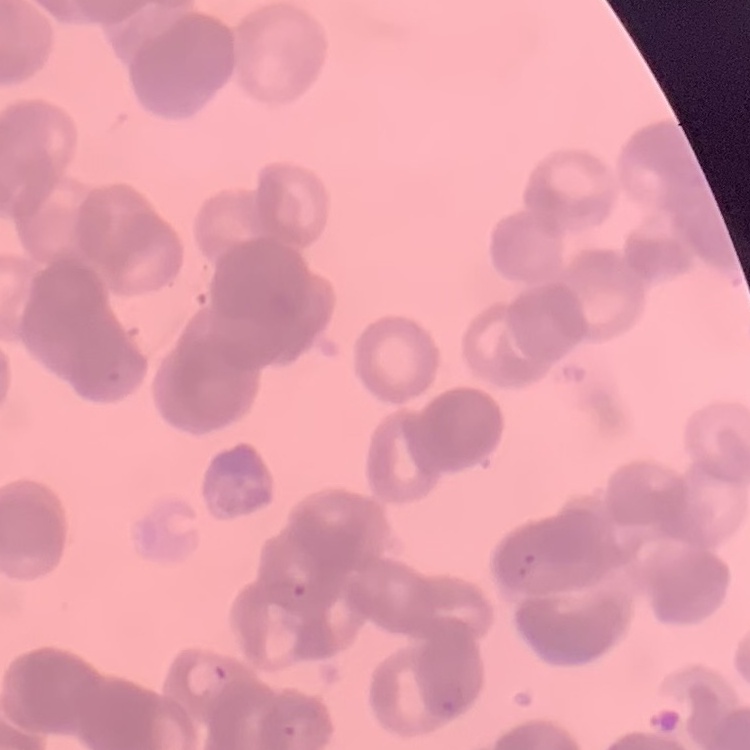
red_blood_cell_morphology: rouleaux formation
preparation: thin blood film
image_type: square crop of a larger photomicrograph
stain: Field's or Giemsa